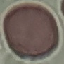

Result: negative for malaria parasites. Thin blood film. Photographed with a smartphone camera at the microscope eyepiece. Giemsa-stained preparation. Cell patch, automatically extracted from a larger field of view and resized to 64 × 64 pixels.